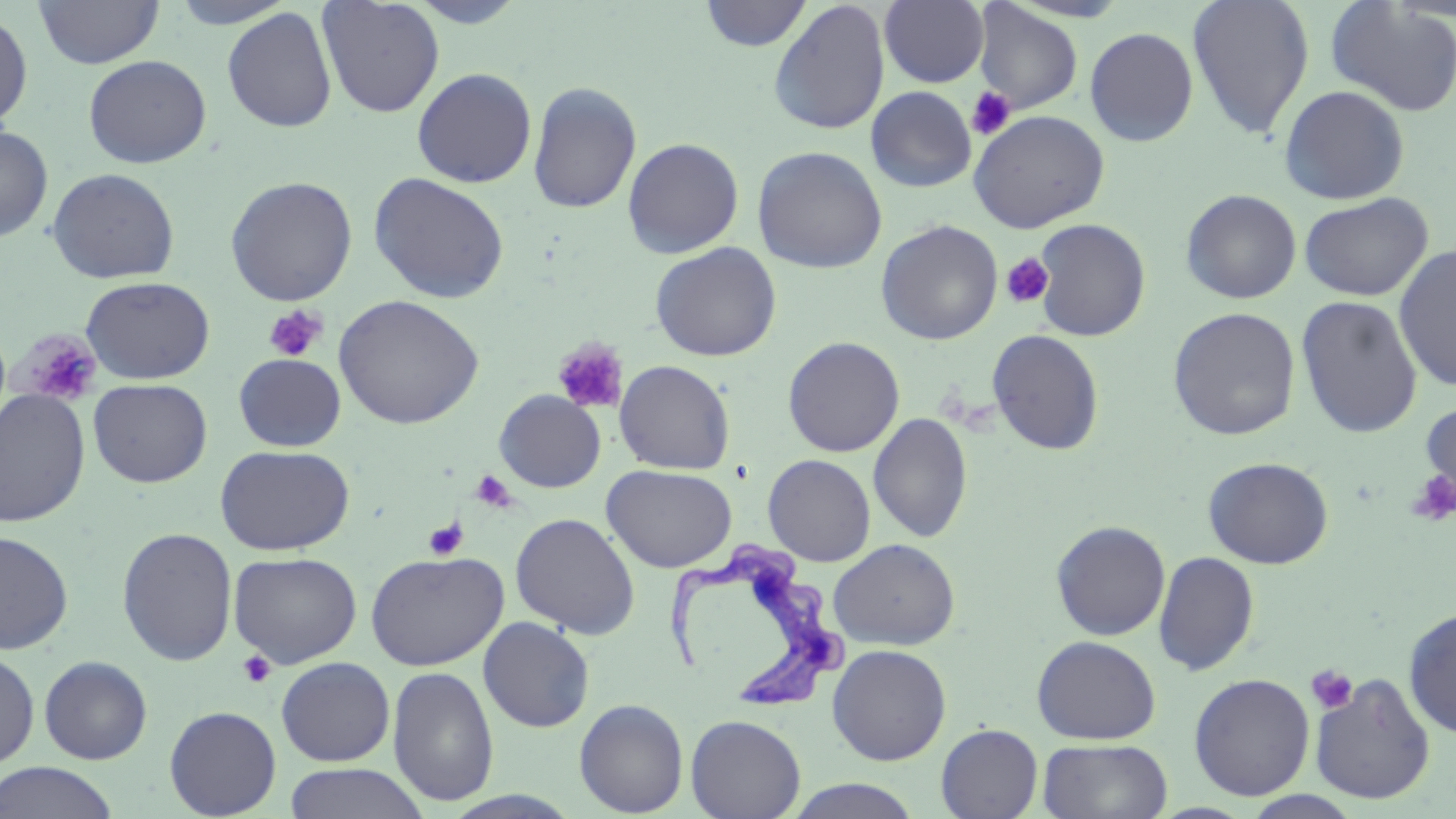
Approximate bounding boxes as (x1, y1, x2, y2) in pixels. Trypanosoma brucei locations: (661, 547, 849, 717). Platelet locations (subset): (966, 87, 1016, 141), (1000, 253, 1055, 308), (264, 305, 327, 362), (16, 330, 102, 407), (552, 338, 629, 415), (470, 469, 516, 513), (1406, 470, 1456, 527), (423, 518, 468, 561), (236, 650, 277, 689), (1306, 666, 1358, 714). Uninfected red blood cell locations (subset): (168, 0, 298, 29), (317, 0, 445, 118), (1187, 0, 1315, 140), (33, 1, 163, 69), (699, 1, 812, 51), (768, 1, 890, 135), (879, 1, 989, 88), (1325, 1, 1456, 116), (972, 3, 1083, 113), (222, 7, 338, 133), (0, 9, 33, 131), (1085, 27, 1198, 147), (83, 54, 211, 169), (412, 67, 537, 188), (527, 81, 642, 214), (1278, 85, 1410, 205), (866, 86, 977, 193), (968, 109, 1109, 233), (0, 124, 53, 243), (623, 137, 744, 258), (752, 146, 887, 274), (46, 167, 180, 284), (369, 172, 510, 304), (225, 176, 358, 306), (1180, 189, 1302, 304), (1299, 192, 1433, 302), (1032, 219, 1151, 341), (876, 220, 1003, 346), (650, 242, 782, 362), (1393, 244, 1456, 391), (80, 275, 215, 385), (333, 294, 484, 430), (1295, 295, 1423, 439), (1167, 307, 1301, 440), (987, 329, 1105, 455), (782, 336, 905, 457), (233, 354, 346, 452), (614, 360, 736, 475), (88, 379, 213, 488), (0, 389, 91, 528), (1418, 397, 1456, 516), (868, 413, 973, 543), (215, 444, 355, 556), (763, 454, 876, 566), (1203, 456, 1334, 569), (602, 464, 737, 572), (510, 513, 641, 639), (1050, 520, 1171, 640), (116, 527, 238, 666), (0, 529, 74, 655), (827, 538, 960, 650), (365, 550, 509, 670), (228, 551, 362, 668), (1153, 551, 1260, 676), (1403, 606, 1456, 739), (478, 617, 594, 732), (1031, 634, 1161, 744), (827, 644, 951, 765), (0, 649, 40, 770), (38, 656, 153, 765), (275, 656, 395, 766), (387, 666, 499, 806), (1188, 673, 1315, 800), (1309, 673, 1436, 805), (574, 698, 688, 817), (164, 705, 282, 818), (685, 714, 806, 819), (935, 723, 1043, 819), (1037, 738, 1173, 819), (0, 762, 121, 819), (283, 763, 431, 819), (783, 778, 925, 819), (1241, 791, 1365, 819). Slide-level diagnosis: Trypanosoma brucei. Light microscopy. Captured at 1000x magnification. May-Grünwald-Giemsa-stained preparation. Thin blood film. Image is 1456×819 pixels. Single field of view.